Locate every uninfected red blood cell.
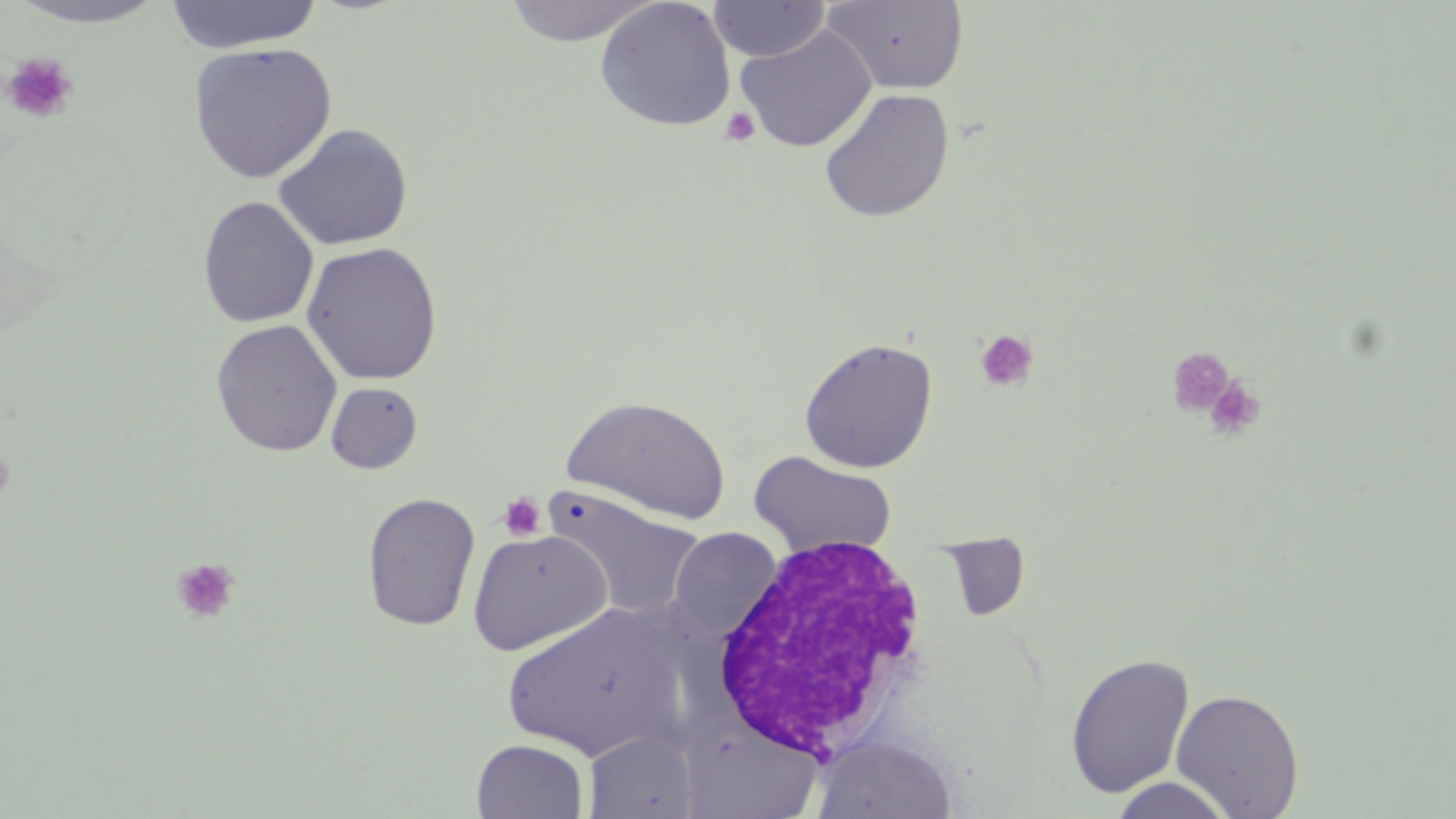

Approximate bounding boxes as (x1,y1)-(x2,y2) corner pairs in pixels.
Uninfected red blood cells: (163,0)-(323,53), (501,0)-(659,46), (596,0)-(736,131), (821,0)-(970,95), (7,1)-(170,28), (707,1)-(830,62), (735,24)-(877,152), (188,42)-(337,184), (819,87)-(955,223), (274,123)-(413,251), (197,196)-(319,328), (301,241)-(443,385), (210,319)-(342,457), (799,337)-(939,473), (326,382)-(423,474), (562,396)-(732,525), (748,450)-(898,559), (546,488)-(705,620), (361,491)-(481,632), (467,528)-(612,655), (668,528)-(781,638), (938,534)-(1031,622), (500,602)-(688,763), (1065,652)-(1195,797), (1170,688)-(1305,817), (678,719)-(825,817), (584,729)-(699,818), (811,733)-(958,818), (471,739)-(590,819), (1107,775)-(1237,818).

White blood cell locations: (708,532)-(936,761). Platelet locations: (1,51)-(79,125), (719,107)-(761,148), (974,329)-(1039,392), (1165,346)-(1236,418), (1203,376)-(1266,441), (0,445)-(17,506), (497,492)-(545,541), (172,557)-(240,624). Slide-level diagnosis: no evidence of blood parasites. May-Grünwald-Giemsa stain. 1000x magnification. Thin blood film. Image is 1456×819 pixels. Single field of view. Optical microscopy.